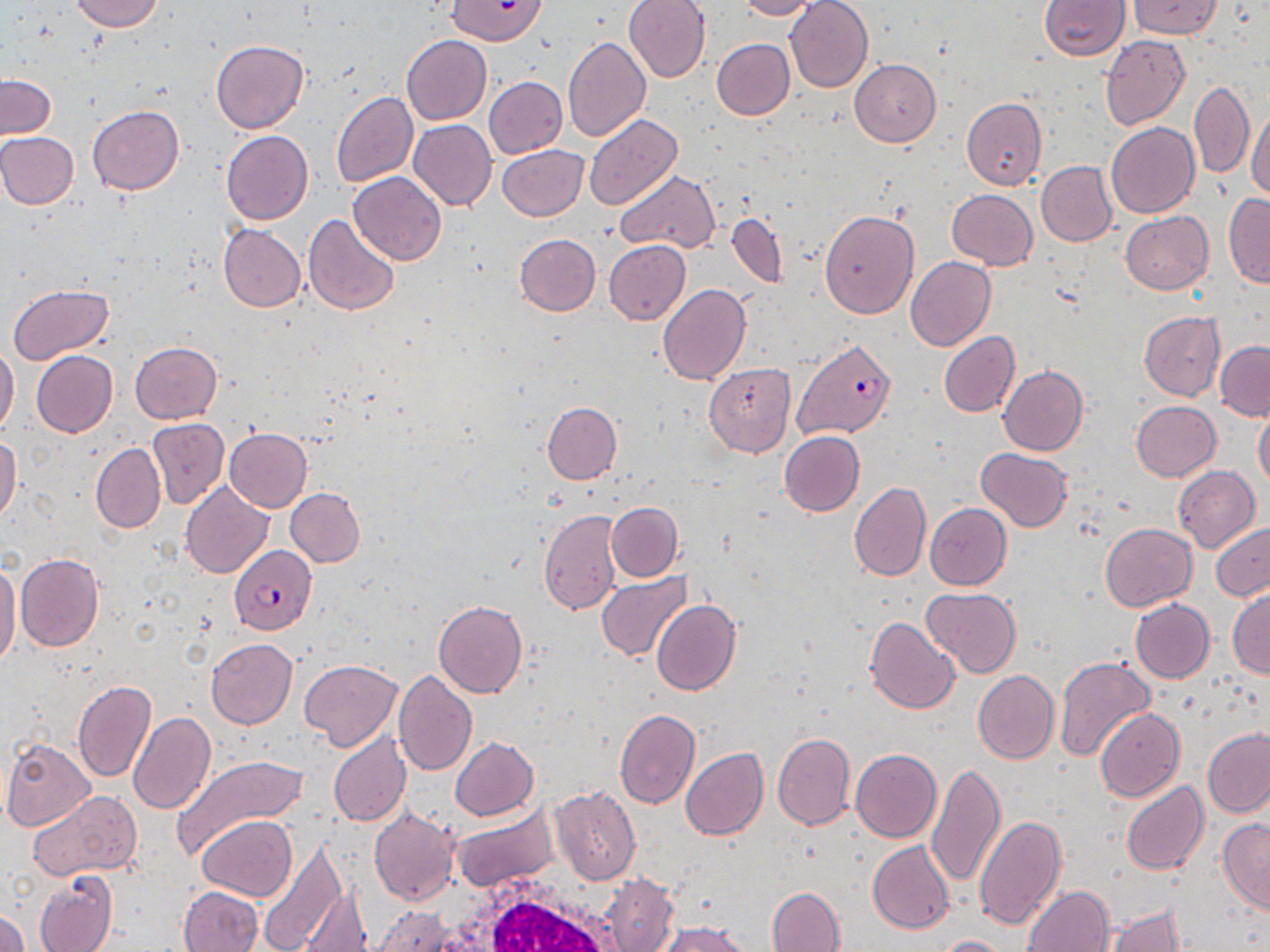
slide-level diagnosis = Plasmodium falciparum
modality = light microscopy
preparation = thin blood film
white blood cell locations = approximate bounding boxes as named x1/y1/x2/y2 corners in pixels: (x1=417, y1=871, x2=636, y2=952)
image size = 1270×952 pixels
stain = May-Grünwald-Giemsa
uninfected red blood cell locations = approximate bounding boxes as named x1/y1/x2/y2 corners in pixels: (x1=68, y1=0, x2=164, y2=33), (x1=446, y1=0, x2=546, y2=46), (x1=624, y1=0, x2=711, y2=82), (x1=736, y1=0, x2=823, y2=20), (x1=785, y1=0, x2=873, y2=91), (x1=1039, y1=0, x2=1129, y2=60), (x1=1129, y1=0, x2=1221, y2=39), (x1=400, y1=35, x2=492, y2=125), (x1=562, y1=35, x2=652, y2=143), (x1=1099, y1=36, x2=1190, y2=129), (x1=711, y1=38, x2=794, y2=120), (x1=211, y1=41, x2=307, y2=134), (x1=848, y1=58, x2=941, y2=147), (x1=1, y1=75, x2=56, y2=139), (x1=484, y1=77, x2=567, y2=159), (x1=1189, y1=80, x2=1254, y2=178), (x1=331, y1=91, x2=419, y2=187), (x1=961, y1=97, x2=1046, y2=192), (x1=1247, y1=101, x2=1270, y2=202), (x1=87, y1=105, x2=185, y2=194), (x1=583, y1=113, x2=683, y2=211), (x1=408, y1=118, x2=496, y2=210), (x1=1105, y1=122, x2=1199, y2=218), (x1=221, y1=130, x2=313, y2=225), (x1=0, y1=132, x2=79, y2=209), (x1=498, y1=145, x2=588, y2=221), (x1=1036, y1=161, x2=1117, y2=247), (x1=615, y1=170, x2=720, y2=252), (x1=348, y1=171, x2=447, y2=266), (x1=946, y1=189, x2=1038, y2=270), (x1=1222, y1=193, x2=1270, y2=288), (x1=819, y1=209, x2=919, y2=319), (x1=1120, y1=211, x2=1214, y2=294), (x1=304, y1=213, x2=400, y2=316), (x1=726, y1=213, x2=788, y2=289), (x1=218, y1=224, x2=304, y2=311), (x1=514, y1=234, x2=601, y2=316), (x1=603, y1=240, x2=690, y2=325), (x1=906, y1=256, x2=995, y2=351), (x1=6, y1=284, x2=113, y2=366), (x1=657, y1=284, x2=750, y2=385), (x1=1138, y1=311, x2=1225, y2=400), (x1=939, y1=332, x2=1020, y2=417), (x1=1215, y1=340, x2=1270, y2=421), (x1=129, y1=342, x2=221, y2=422), (x1=0, y1=345, x2=19, y2=437), (x1=32, y1=351, x2=118, y2=437), (x1=703, y1=364, x2=796, y2=457), (x1=999, y1=365, x2=1088, y2=455), (x1=542, y1=401, x2=621, y2=484), (x1=1131, y1=401, x2=1221, y2=482), (x1=1253, y1=407, x2=1270, y2=489), (x1=147, y1=418, x2=228, y2=508), (x1=223, y1=428, x2=312, y2=512), (x1=779, y1=430, x2=864, y2=516), (x1=0, y1=435, x2=22, y2=522), (x1=91, y1=443, x2=165, y2=533), (x1=975, y1=447, x2=1071, y2=532), (x1=1173, y1=466, x2=1260, y2=553), (x1=180, y1=481, x2=273, y2=578), (x1=849, y1=482, x2=931, y2=581), (x1=285, y1=487, x2=364, y2=567), (x1=606, y1=502, x2=682, y2=581), (x1=924, y1=503, x2=1011, y2=590), (x1=539, y1=509, x2=624, y2=616), (x1=1210, y1=522, x2=1270, y2=602), (x1=1099, y1=523, x2=1197, y2=611), (x1=15, y1=554, x2=103, y2=652), (x1=0, y1=559, x2=21, y2=671), (x1=596, y1=572, x2=692, y2=661), (x1=921, y1=586, x2=1022, y2=678), (x1=1227, y1=587, x2=1270, y2=678), (x1=1129, y1=598, x2=1214, y2=683), (x1=433, y1=599, x2=527, y2=698), (x1=650, y1=599, x2=740, y2=695), (x1=865, y1=616, x2=959, y2=714), (x1=206, y1=638, x2=297, y2=729), (x1=1054, y1=655, x2=1155, y2=763), (x1=299, y1=660, x2=403, y2=751), (x1=392, y1=669, x2=478, y2=777), (x1=973, y1=670, x2=1059, y2=764), (x1=72, y1=681, x2=156, y2=784), (x1=1094, y1=707, x2=1184, y2=802), (x1=614, y1=708, x2=699, y2=809), (x1=127, y1=712, x2=215, y2=815), (x1=1203, y1=727, x2=1270, y2=819), (x1=328, y1=732, x2=411, y2=828), (x1=773, y1=733, x2=855, y2=831), (x1=450, y1=737, x2=538, y2=820), (x1=1, y1=738, x2=97, y2=831), (x1=680, y1=748, x2=767, y2=841), (x1=851, y1=749, x2=941, y2=844), (x1=172, y1=755, x2=307, y2=861), (x1=926, y1=761, x2=1007, y2=889), (x1=1122, y1=782, x2=1208, y2=877), (x1=551, y1=786, x2=641, y2=885), (x1=28, y1=790, x2=143, y2=879), (x1=452, y1=806, x2=556, y2=892), (x1=368, y1=807, x2=461, y2=907), (x1=973, y1=814, x2=1067, y2=931), (x1=197, y1=815, x2=297, y2=901), (x1=1218, y1=817, x2=1270, y2=913), (x1=866, y1=840, x2=953, y2=934), (x1=255, y1=841, x2=347, y2=952), (x1=33, y1=871, x2=118, y2=952), (x1=602, y1=875, x2=679, y2=952), (x1=298, y1=883, x2=371, y2=952), (x1=1023, y1=885, x2=1113, y2=952), (x1=179, y1=886, x2=264, y2=952), (x1=767, y1=887, x2=845, y2=952), (x1=1105, y1=905, x2=1186, y2=952), (x1=370, y1=907, x2=457, y2=951), (x1=0, y1=909, x2=29, y2=952), (x1=658, y1=921, x2=748, y2=952), (x1=929, y1=935, x2=1014, y2=952)
field of view = single
magnification = 1000x
Plasmodium falciparum-infected red blood cell locations = approximate bounding boxes as named x1/y1/x2/y2 corners in pixels: (x1=793, y1=339, x2=895, y2=439), (x1=230, y1=545, x2=315, y2=635)